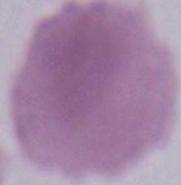
Photomicrograph. An erythrocyte is shown. Captured at 1000x magnification.